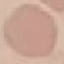

Result: no malaria parasites detected. Cell patch, automatically extracted from a larger field of view and resized to 64 × 64 pixels. Thin blood smear. Photographed with a smartphone camera at the microscope eyepiece. Giemsa-stained preparation.